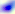

Captured at 400x magnification. Photomicrograph. Toxoplasma gondii is seen.